Identify the parasite.
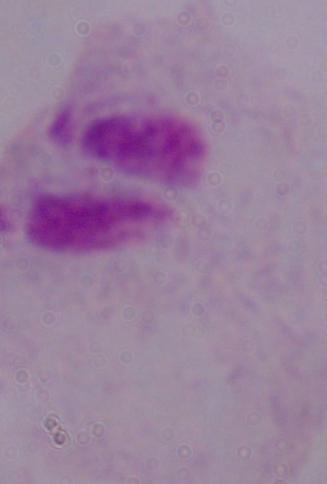

This is a trichomonad.

magnification = 1000x
modality = photomicrograph